Outline each blood parasite and name the species.
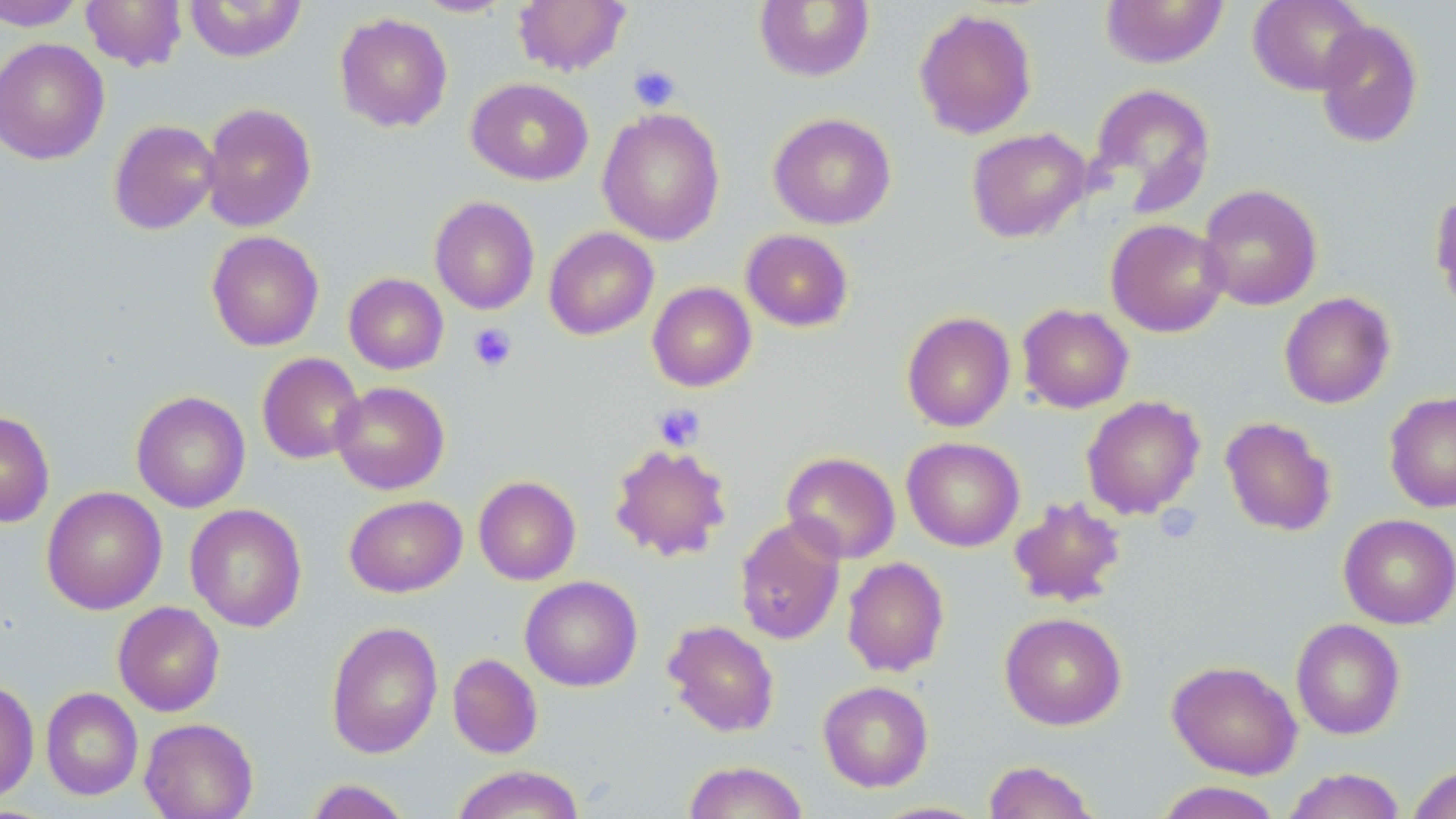
No blood parasites observed.

slide-level diagnosis = no evidence of blood parasites
magnification = 1000x
image size = 1456×819 pixels
stain = May-Grünwald-Giemsa
uninfected red blood cell locations = approximate bounding boxes as [x1, y1, x2, y2] in pixels: [1, 0, 87, 31], [81, 0, 187, 72], [184, 0, 307, 62], [412, 0, 514, 17], [1100, 0, 1229, 69], [1247, 0, 1371, 95], [513, 1, 630, 76], [754, 1, 875, 83], [914, 8, 1037, 139], [334, 12, 453, 133], [1313, 19, 1424, 149], [0, 38, 109, 165], [466, 78, 593, 185], [1087, 83, 1216, 216], [200, 102, 317, 232], [597, 108, 725, 246], [768, 112, 896, 230], [108, 119, 220, 235], [966, 127, 1092, 243], [1197, 183, 1323, 310], [1428, 187, 1456, 314], [429, 196, 539, 315], [1105, 218, 1229, 337], [544, 227, 659, 340], [740, 229, 854, 332], [206, 231, 324, 352], [343, 273, 449, 374], [647, 282, 757, 392], [1279, 292, 1396, 409], [1017, 304, 1134, 413], [901, 311, 1016, 432], [257, 352, 366, 464], [331, 381, 449, 495], [131, 391, 250, 513], [1384, 391, 1456, 513], [1081, 396, 1205, 519], [0, 410, 55, 528], [1220, 416, 1337, 536], [901, 436, 1025, 552], [608, 443, 733, 562], [781, 451, 901, 564], [473, 476, 581, 585], [41, 486, 167, 615], [344, 495, 467, 597], [1008, 495, 1127, 608], [185, 503, 307, 632], [1338, 513, 1456, 630], [734, 516, 846, 645], [842, 557, 950, 676], [520, 575, 642, 692], [112, 601, 225, 716], [999, 611, 1127, 731], [1291, 618, 1406, 740], [326, 620, 443, 759], [663, 620, 779, 737], [447, 653, 543, 759], [1166, 660, 1303, 779], [0, 679, 40, 804], [818, 680, 934, 792], [41, 687, 143, 800], [139, 718, 258, 819], [682, 760, 809, 819], [982, 760, 1100, 819], [1406, 763, 1456, 819], [450, 765, 586, 819], [1281, 767, 1407, 819], [303, 779, 414, 819], [1152, 781, 1284, 819], [871, 801, 991, 818]
modality = optical microscopy
preparation = thin blood film
field of view = one of a larger specimen
platelet locations = approximate bounding boxes as [x1, y1, x2, y2] in pixels: [628, 65, 680, 111], [468, 322, 517, 372], [652, 403, 706, 451], [1156, 503, 1201, 543]